Classify this cell by malaria status.
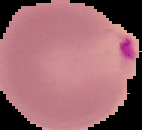
Parasitized.

Segmented cell region on a black background. From a thin blood smear. Image is 142×130 pixels.